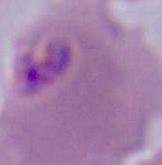

modality = photomicrograph
identification = Plasmodium
magnification = 400x or 1000x